Report the malaria status of this cell.
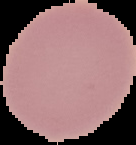
Uninfected.

Summary:
  - Image type: segmented cell region with the area outside set to black
  - Image size: 136×145 pixels
  - Preparation: thin blood smear